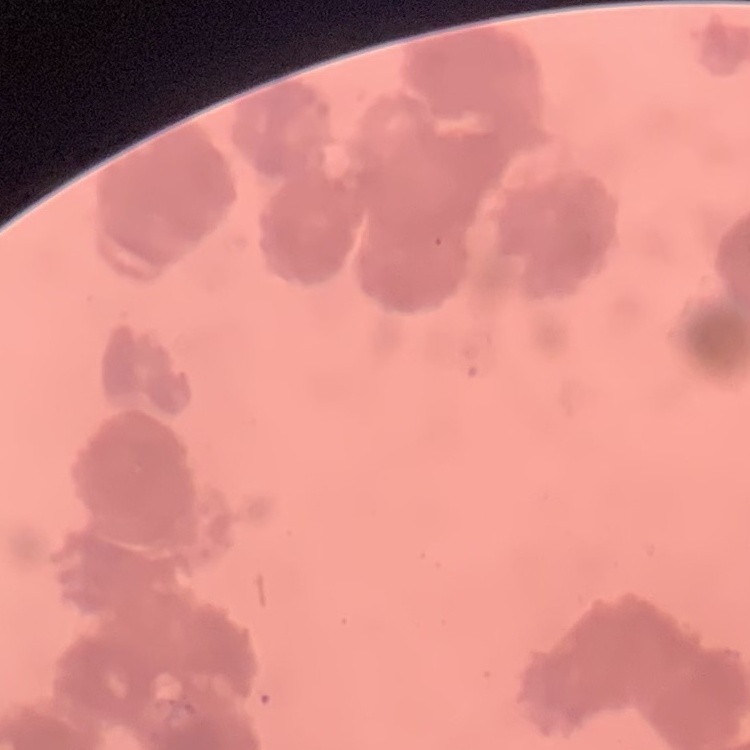
Summary:
  - Red blood cell morphology: rouleaux formation
  - Preparation: thin blood film
  - Image type: square crop of a larger photomicrograph
  - Stain: Field's or Giemsa